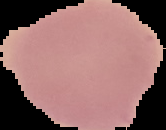
Segmented cell region on a black background. Image is 166×130 pixels. From a thin blood smear. Result: malaria parasites identified.